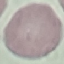

Summary:
  - Malaria status: uninfected
  - Stain: Giemsa
  - Capture: smartphone camera at the microscope eyepiece
  - Preparation: thin smear
  - Image type: cell patch, automatically extracted from a larger field of view and resized to 64 × 64 pixels